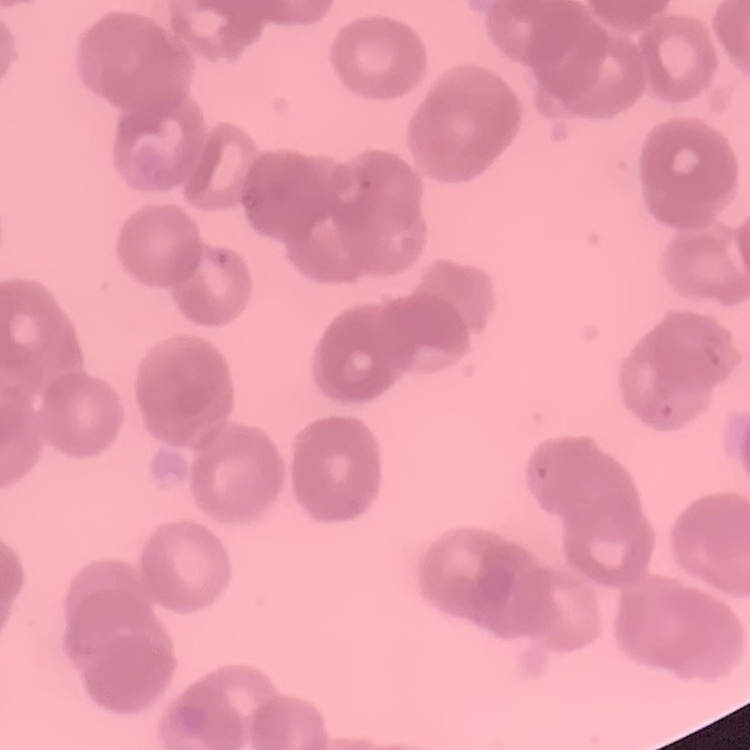 The erythrocytes exhibit rouleaux formation. Thin peripheral smear. Square crop of a larger photomicrograph. Stained with either Field's or Giemsa.